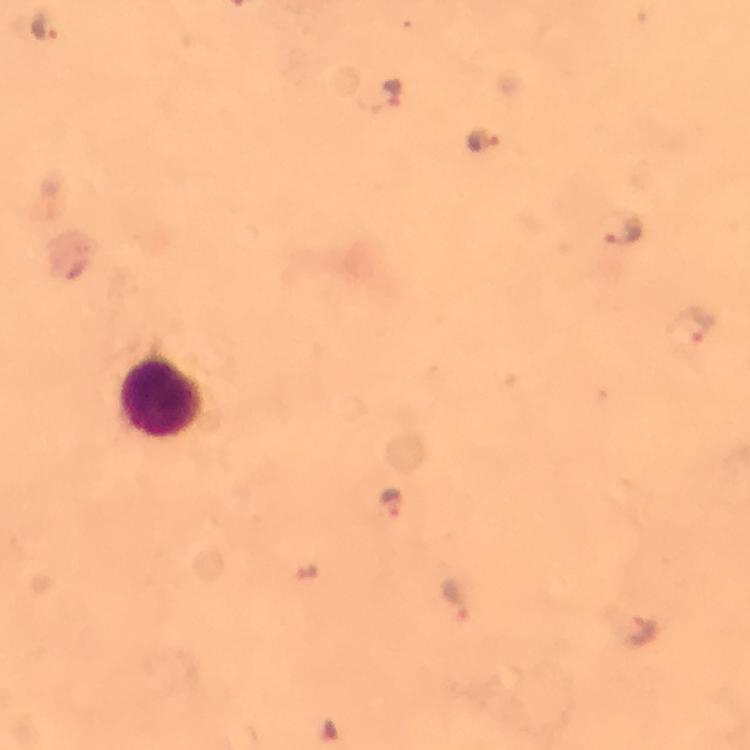
{
  "magnification": "100x",
  "immersion_oil": "applied",
  "stain": "Giemsa",
  "plasmodium_parasite_locations": "approximate centers as (x, y) in pixels: (44, 26), (392, 89), (484, 143), (623, 227), (696, 324), (394, 502), (455, 599), (645, 630)",
  "capture": "smartphone mounted on the microscope",
  "cropped_from": "a single field of view",
  "image_size": "750×750 pixels",
  "leukocyte_locations": "approximate centers as (x, y) in pixels: (165, 395)",
  "preparation": "thick smear",
  "context": "from a malaria diagnostic workup"
}